State which parasite is depicted.
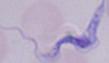

This is a trypanosome.

Summary:
  - Magnification: 1000x
  - Modality: photomicrograph